Describe the morphology of the erythrocytes.
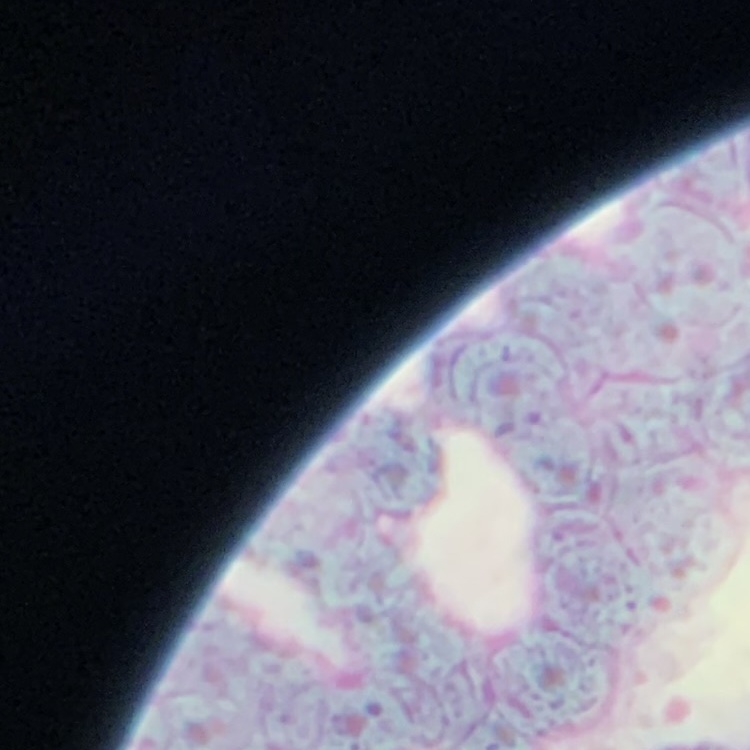
Rouleaux formation.

One tile cut from a larger photomicrograph. Thin blood smear. Stained with either Field's or Giemsa.